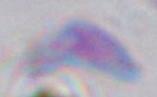
Summary:
  - Modality: micrograph
  - Magnification: 1000x
  - Identification: Toxoplasma gondii